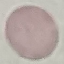
Summary:
  - Malaria status: uninfected
  - Image type: cell patch, automatically extracted from a larger field of view and resized to 64 × 64 pixels
  - Preparation: thin blood smear
  - Capture: smartphone camera at the microscope eyepiece
  - Stain: Giemsa